Assess for malaria.
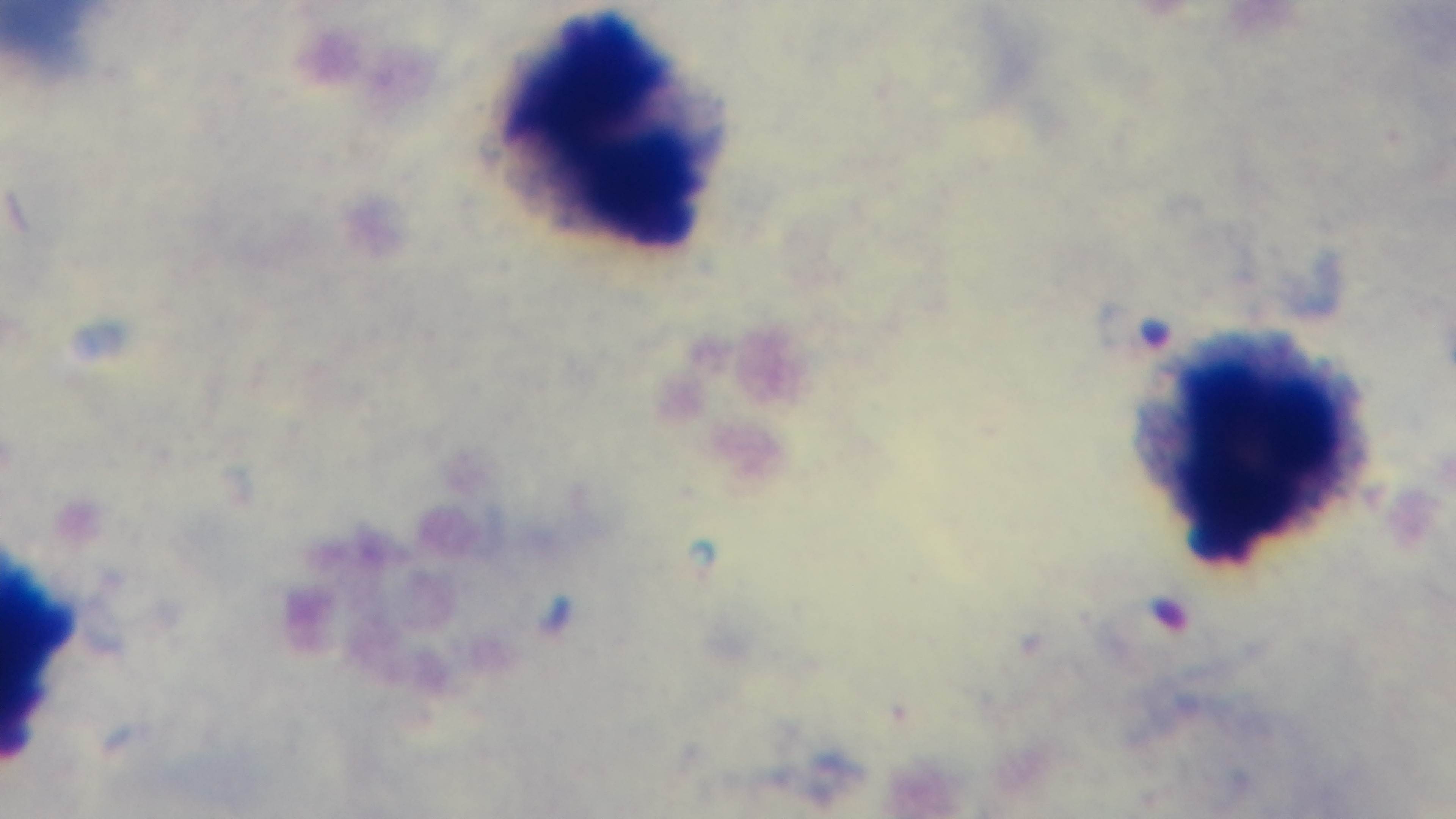
It is infected.

{
  "objective": "100x oil immersion",
  "capture": "mounted 4K digital camera",
  "preparation": "thick blood film",
  "modality": "light microscopy",
  "field_of_view": "one from the slide",
  "stain": "Giemsa"
}